Report the malaria status of this cell.
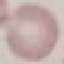

It is uninfected.

Summary:
  - Preparation: thin smear
  - Image type: automatically extracted cell patch, resized to 64 × 64 pixels
  - Capture: smartphone through the microscope eyepiece
  - Stain: Giemsa